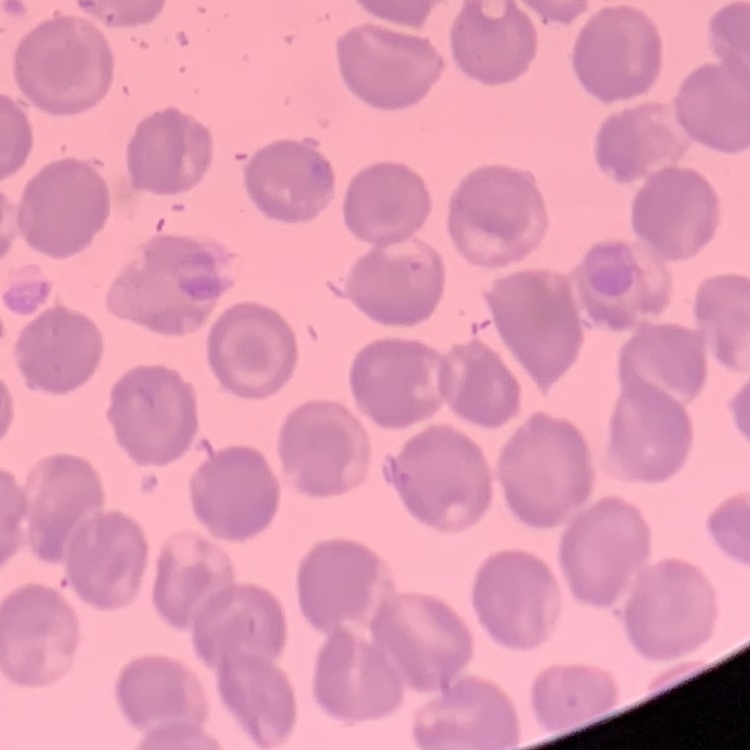

red blood cell morphology = no rouleaux formation
preparation = thin peripheral smear
image type = one tile cut from a larger photomicrograph
stain = Field's or Giemsa